Locate every blood parasite and identify its species.
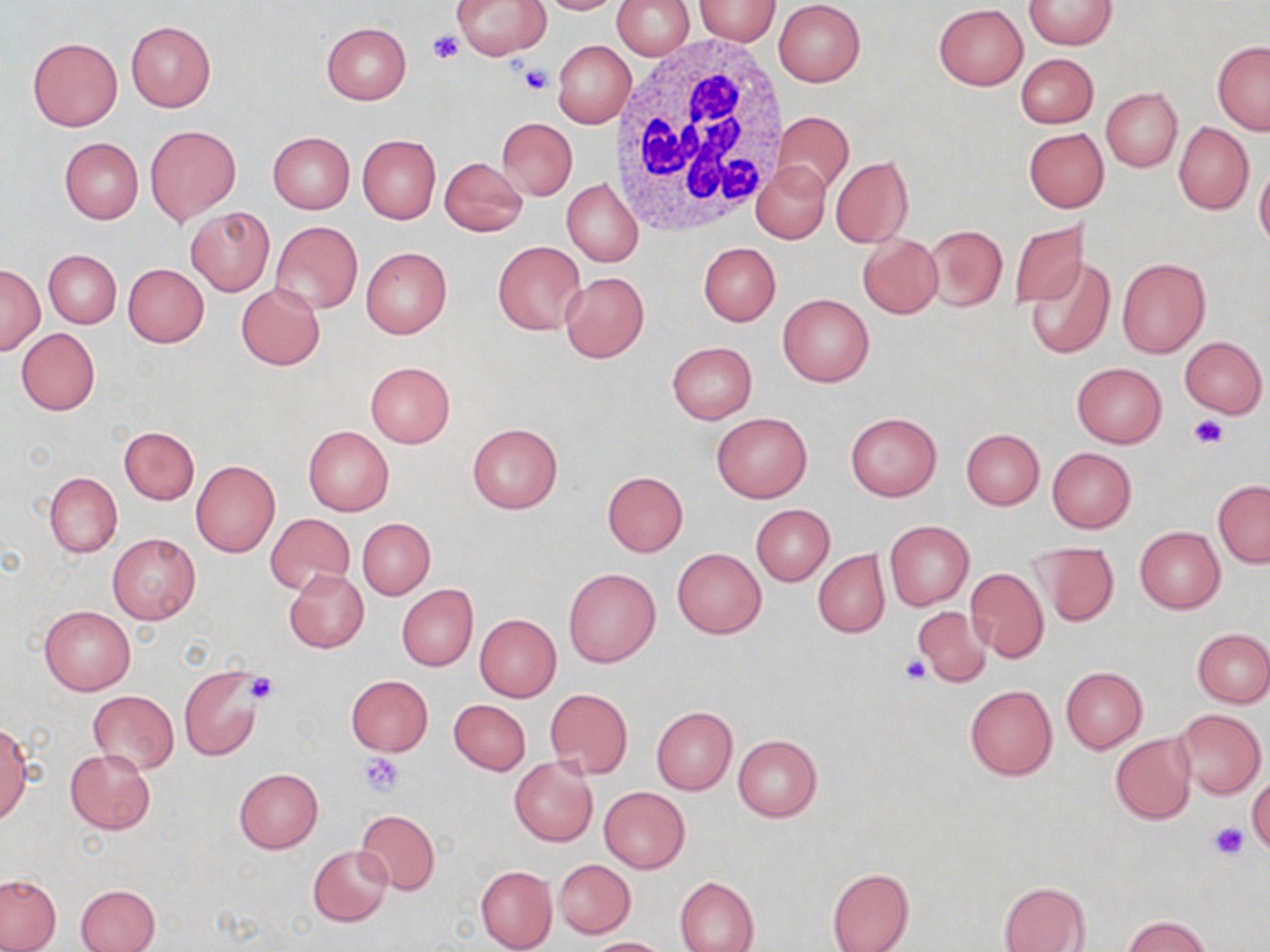

No blood parasites seen.

Approximate bounding boxes as [x1, y1, x2, y2] in pixels. White blood cell locations: [611, 39, 794, 234]. Platelet locations: [427, 30, 463, 66], [520, 64, 555, 96], [1188, 414, 1226, 448], [901, 655, 932, 684], [247, 672, 280, 704], [359, 753, 406, 796], [1209, 822, 1246, 858]. Uninfected red blood cell locations: [453, 0, 550, 60], [533, 0, 625, 15], [611, 0, 694, 60], [694, 0, 780, 44], [1024, 0, 1115, 49], [773, 1, 865, 87], [934, 4, 1027, 90], [126, 20, 215, 112], [321, 22, 411, 104], [27, 37, 122, 132], [551, 40, 635, 128], [1212, 41, 1270, 134], [1015, 53, 1097, 129], [1101, 89, 1182, 171], [772, 112, 854, 200], [496, 119, 577, 200], [1173, 121, 1253, 214], [145, 125, 240, 224], [1023, 128, 1109, 213], [268, 131, 354, 214], [358, 134, 440, 224], [59, 137, 143, 224], [438, 156, 528, 236], [831, 156, 914, 247], [753, 161, 830, 244], [1254, 162, 1270, 251], [561, 179, 643, 267], [186, 207, 273, 296], [1009, 219, 1089, 310], [271, 221, 363, 314], [925, 225, 1007, 312], [858, 234, 943, 319], [493, 241, 587, 336], [698, 243, 780, 326], [361, 246, 452, 338], [44, 250, 121, 328], [1025, 256, 1116, 359], [1116, 257, 1211, 358], [123, 263, 209, 347], [0, 264, 44, 354], [560, 271, 648, 362], [235, 284, 325, 370], [778, 294, 874, 387], [16, 328, 100, 415], [1180, 336, 1267, 418], [667, 342, 757, 423], [364, 362, 455, 449], [1071, 362, 1166, 448], [845, 411, 942, 501], [712, 412, 811, 502], [466, 422, 563, 514], [119, 426, 200, 504], [303, 426, 394, 516], [960, 428, 1045, 510], [1047, 447, 1137, 533], [191, 460, 280, 556], [602, 470, 688, 556], [44, 472, 122, 556], [1213, 481, 1270, 567], [751, 503, 834, 586], [266, 513, 355, 594], [357, 518, 435, 600], [884, 521, 973, 609], [1134, 526, 1224, 613], [108, 532, 201, 624], [1031, 540, 1119, 624], [672, 547, 766, 638], [813, 550, 890, 638], [965, 565, 1049, 663], [284, 568, 369, 653], [563, 568, 661, 668], [397, 584, 478, 671], [39, 605, 136, 696], [914, 606, 991, 687], [474, 614, 561, 701], [1193, 629, 1270, 706], [1060, 666, 1146, 752], [180, 667, 264, 761], [345, 675, 433, 757], [964, 685, 1058, 781], [545, 688, 632, 778], [88, 691, 178, 774], [448, 698, 531, 774], [652, 707, 736, 794], [1172, 708, 1266, 800], [0, 723, 31, 823], [1110, 733, 1195, 824], [733, 734, 822, 821], [65, 749, 155, 834], [509, 757, 597, 847], [234, 767, 323, 852], [1248, 775, 1270, 855], [598, 786, 690, 874], [356, 810, 441, 895], [309, 844, 393, 927], [554, 860, 635, 937], [476, 865, 557, 951], [827, 868, 913, 952], [0, 875, 61, 951], [675, 876, 760, 952], [998, 881, 1091, 952], [74, 883, 159, 952], [1122, 915, 1214, 952], [585, 937, 671, 951]. Slide-level diagnosis: negative for blood parasites. Single field of view. May-Grünwald-Giemsa-stained preparation. Image is 1270×952 pixels. Captured at 1000x magnification. Optical microscopy. Thin blood film.